Classify this cell by malaria status.
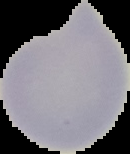

It is uninfected.

Cell region segmented out of the field of view; the surrounding area is masked to black. From a thin blood film. Image is 130×154 pixels.